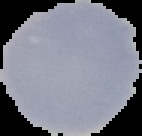
preparation = thin blood film
image size = 142×136 pixels
image type = segmented cell region with the area outside set to black
result = no malaria parasites seen